Give the extent of all Plasmodium vivax-infected red blood cells.
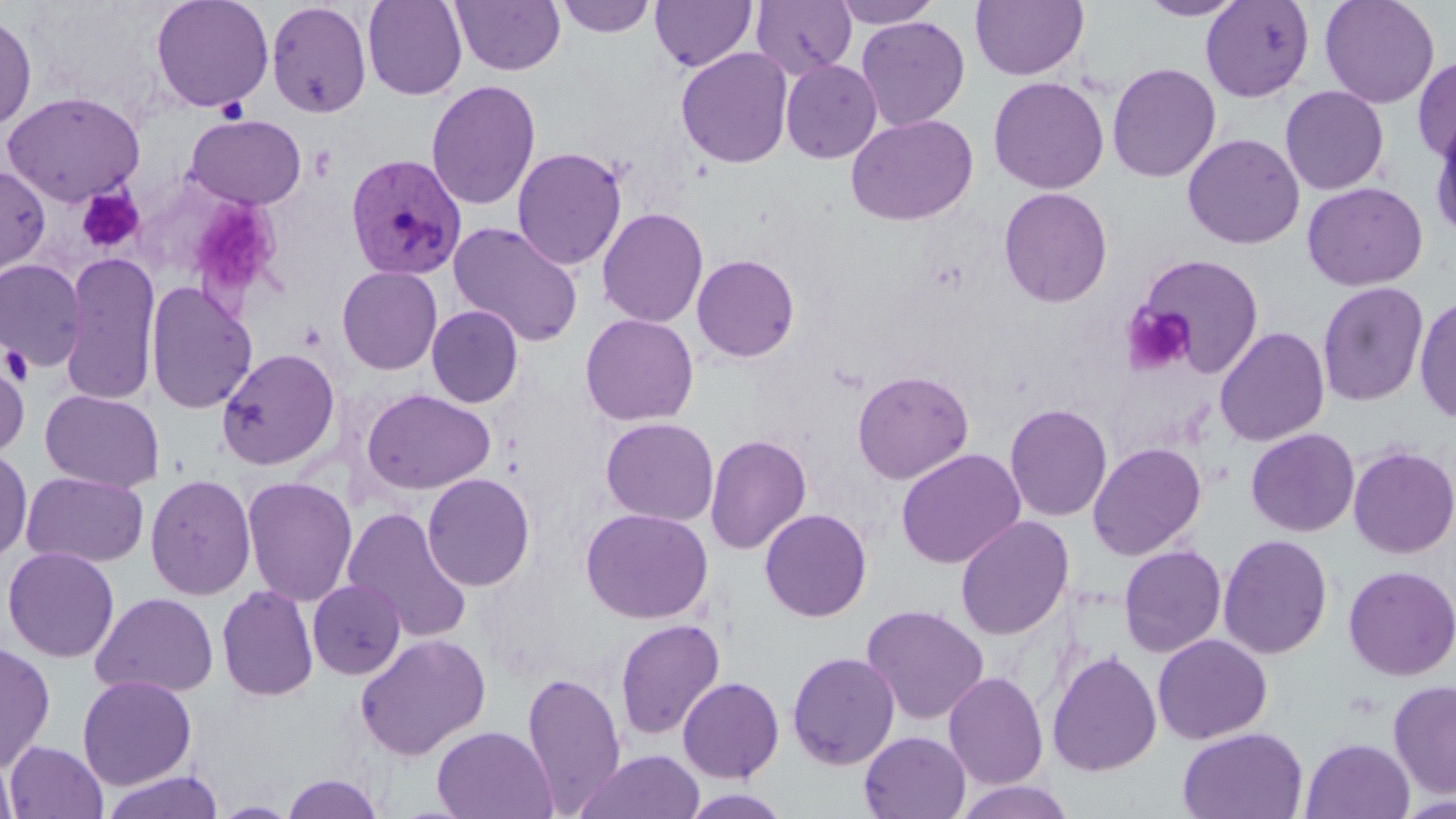
Approximate bounding boxes as named x1/y1/x2/y2 corners in pixels.
Plasmodium vivax-infected red blood cells: (x1=344, y1=153, x2=466, y2=281).

slide-level diagnosis = Plasmodium vivax
preparation = thin blood film
uninfected red blood cell locations = approximate bounding boxes as named x1/y1/x2/y2 corners in pixels: (x1=150, y1=0, x2=274, y2=113), (x1=362, y1=0, x2=468, y2=101), (x1=452, y1=0, x2=566, y2=76), (x1=555, y1=0, x2=656, y2=38), (x1=650, y1=0, x2=757, y2=72), (x1=750, y1=0, x2=857, y2=78), (x1=831, y1=0, x2=943, y2=28), (x1=970, y1=0, x2=1089, y2=81), (x1=1137, y1=0, x2=1248, y2=22), (x1=1319, y1=0, x2=1440, y2=109), (x1=1200, y1=1, x2=1314, y2=102), (x1=266, y1=2, x2=373, y2=119), (x1=0, y1=11, x2=37, y2=133), (x1=856, y1=16, x2=971, y2=131), (x1=676, y1=47, x2=794, y2=169), (x1=1412, y1=56, x2=1456, y2=165), (x1=780, y1=59, x2=882, y2=164), (x1=1106, y1=62, x2=1221, y2=183), (x1=988, y1=76, x2=1109, y2=194), (x1=426, y1=80, x2=541, y2=211), (x1=1280, y1=85, x2=1390, y2=196), (x1=1, y1=90, x2=146, y2=207), (x1=845, y1=113, x2=978, y2=226), (x1=185, y1=114, x2=307, y2=210), (x1=1429, y1=115, x2=1456, y2=242), (x1=1182, y1=133, x2=1305, y2=250), (x1=512, y1=147, x2=627, y2=271), (x1=0, y1=166, x2=50, y2=279), (x1=1302, y1=181, x2=1427, y2=291), (x1=998, y1=187, x2=1113, y2=308), (x1=597, y1=207, x2=709, y2=328), (x1=447, y1=221, x2=584, y2=347), (x1=60, y1=251, x2=161, y2=407), (x1=692, y1=254, x2=800, y2=362), (x1=1138, y1=254, x2=1264, y2=376), (x1=0, y1=259, x2=87, y2=371), (x1=336, y1=266, x2=443, y2=375), (x1=145, y1=281, x2=257, y2=415), (x1=1316, y1=281, x2=1430, y2=407), (x1=1414, y1=293, x2=1456, y2=424), (x1=426, y1=304, x2=524, y2=408), (x1=580, y1=313, x2=699, y2=426), (x1=1214, y1=326, x2=1330, y2=447), (x1=216, y1=348, x2=339, y2=470), (x1=0, y1=354, x2=30, y2=462), (x1=852, y1=369, x2=974, y2=484), (x1=40, y1=389, x2=165, y2=493), (x1=361, y1=389, x2=496, y2=495), (x1=1004, y1=404, x2=1113, y2=522), (x1=600, y1=417, x2=719, y2=526), (x1=1245, y1=428, x2=1360, y2=537), (x1=705, y1=434, x2=812, y2=554), (x1=1088, y1=442, x2=1207, y2=560), (x1=1348, y1=445, x2=1456, y2=559), (x1=0, y1=447, x2=33, y2=565), (x1=895, y1=448, x2=1026, y2=569), (x1=21, y1=470, x2=149, y2=567), (x1=145, y1=473, x2=256, y2=600), (x1=422, y1=473, x2=536, y2=591), (x1=241, y1=476, x2=358, y2=606), (x1=342, y1=507, x2=474, y2=644), (x1=580, y1=507, x2=713, y2=624), (x1=759, y1=508, x2=872, y2=622), (x1=955, y1=515, x2=1075, y2=641), (x1=1217, y1=533, x2=1334, y2=659), (x1=1118, y1=545, x2=1227, y2=658), (x1=2, y1=546, x2=120, y2=663), (x1=1211, y1=551, x2=1453, y2=667), (x1=1342, y1=565, x2=1456, y2=681), (x1=307, y1=580, x2=406, y2=680), (x1=216, y1=585, x2=319, y2=702), (x1=90, y1=592, x2=219, y2=698), (x1=861, y1=604, x2=989, y2=726), (x1=614, y1=619, x2=726, y2=740), (x1=354, y1=633, x2=491, y2=760), (x1=1152, y1=634, x2=1272, y2=744), (x1=0, y1=640, x2=56, y2=773), (x1=1047, y1=650, x2=1162, y2=777), (x1=786, y1=651, x2=901, y2=770), (x1=521, y1=670, x2=626, y2=813), (x1=943, y1=671, x2=1049, y2=790), (x1=77, y1=675, x2=197, y2=789), (x1=677, y1=677, x2=785, y2=783), (x1=1388, y1=679, x2=1456, y2=798), (x1=431, y1=725, x2=557, y2=819), (x1=1178, y1=727, x2=1308, y2=819), (x1=859, y1=731, x2=971, y2=819), (x1=1300, y1=737, x2=1415, y2=819), (x1=5, y1=741, x2=108, y2=819), (x1=0, y1=746, x2=19, y2=819), (x1=572, y1=750, x2=705, y2=819), (x1=97, y1=770, x2=226, y2=819), (x1=281, y1=772, x2=384, y2=818), (x1=952, y1=780, x2=1077, y2=818), (x1=679, y1=788, x2=793, y2=818), (x1=211, y1=801, x2=301, y2=818)
magnification = 1000x
stain = May-Grünwald-Giemsa
field of view = single
modality = optical microscopy
platelet locations = approximate bounding boxes as named x1/y1/x2/y2 corners in pixels: (x1=216, y1=97, x2=248, y2=124), (x1=76, y1=187, x2=144, y2=253), (x1=183, y1=195, x2=284, y2=304), (x1=1123, y1=304, x2=1195, y2=375), (x1=1, y1=344, x2=34, y2=384)
image size = 1456×819 pixels